Assess for malaria.
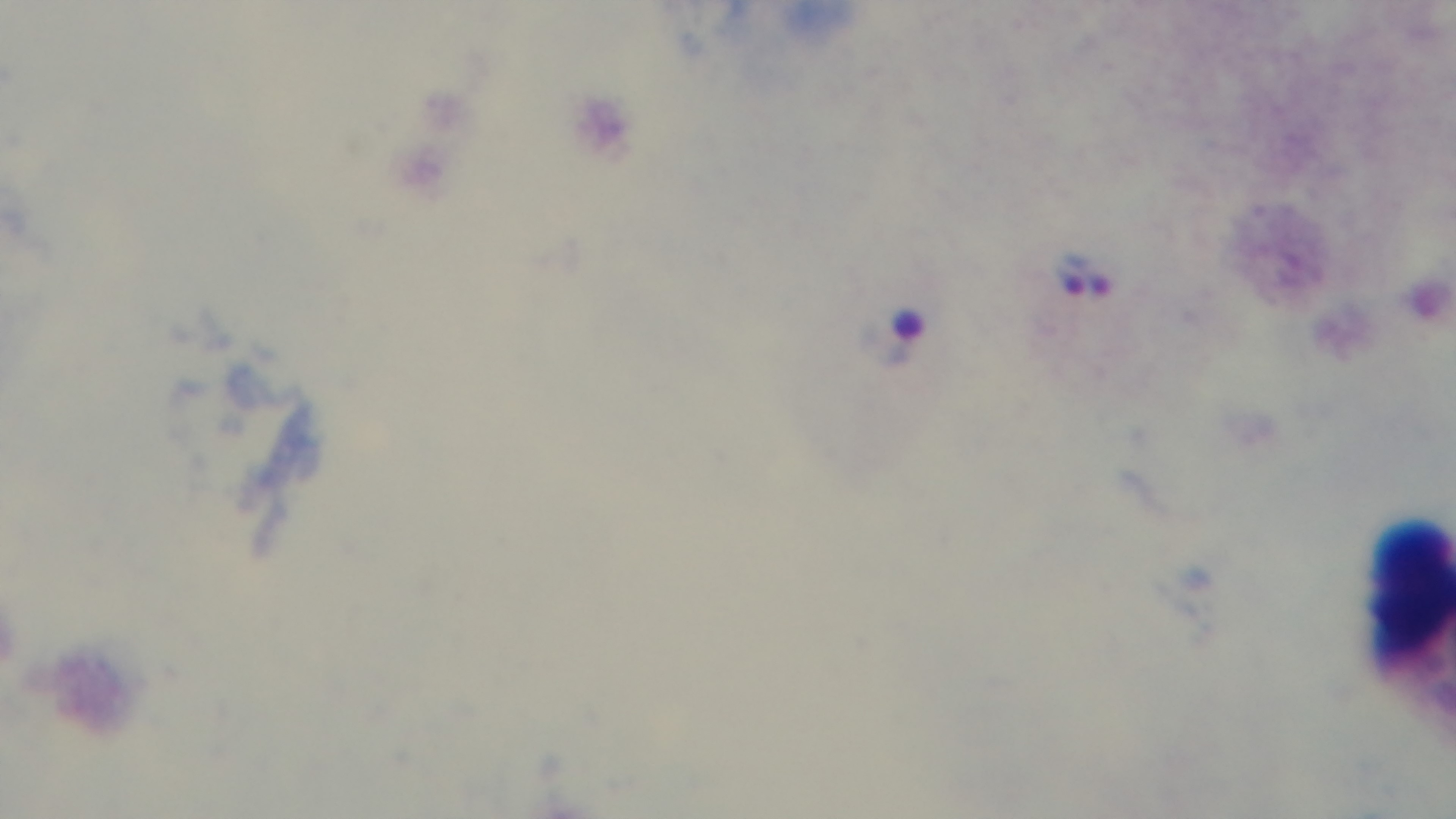

Positive.

Summary:
  - Stain: Giemsa
  - Objective: 100x oil immersion
  - Field of view: single
  - Modality: light microscopy
  - Preparation: thick blood film
  - Capture: mounted 4K digital camera